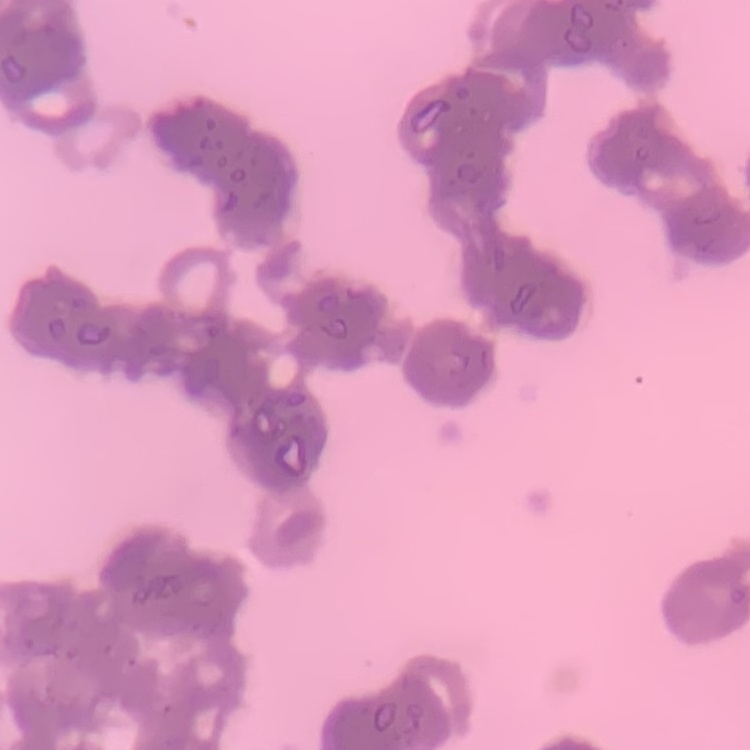

The red blood cells show rouleaux formation. Thin peripheral smear. Field's or Giemsa stain. One tile cut from a larger photomicrograph.